Classify this cell by malaria status.
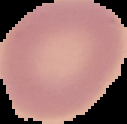

Uninfected.

Summary:
  - Image size: 127×124 pixels
  - Image type: cell region segmented out of the field of view; surrounding area masked to black
  - Preparation: thin blood film